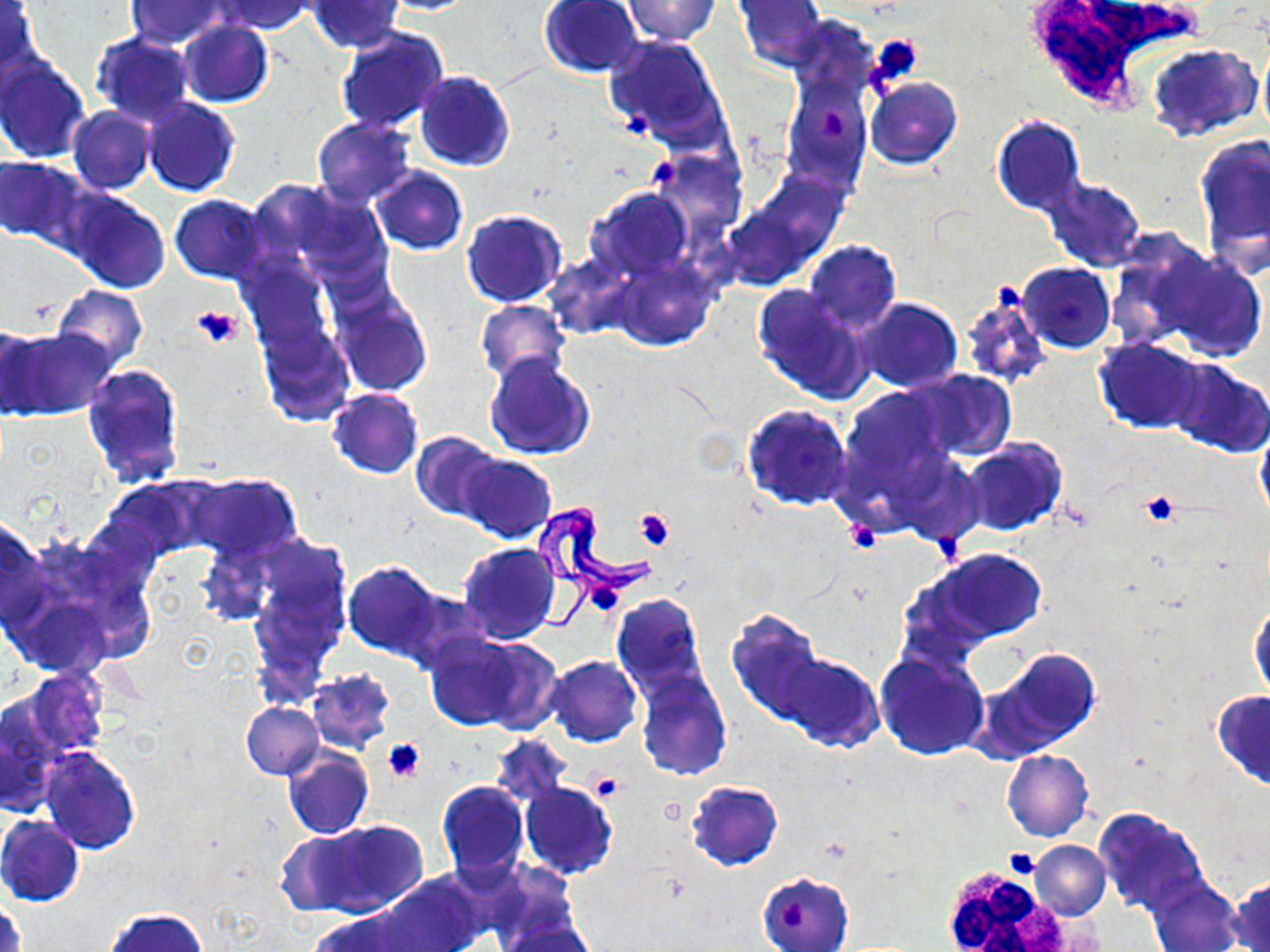

Summary:
  - Coordinate format: approximate bounding boxes as (x1,y1)-(x2,y2) corner pairs in pixels
  - Platelet locations: (866,34)-(921,91), (623,107)-(654,136), (824,109)-(845,138), (648,158)-(680,186), (994,282)-(1023,311), (192,304)-(245,349), (1139,490)-(1183,528), (635,508)-(676,549), (844,520)-(882,554), (933,532)-(965,559), (589,580)-(621,612), (383,739)-(425,782), (588,772)-(625,803), (656,799)-(686,826), (1003,847)-(1042,881), (780,897)-(812,931)
  - Uninfected red blood cell locations: (214,0)-(316,35), (376,0)-(481,15), (622,0)-(718,44), (732,0)-(828,72), (125,1)-(230,47), (307,1)-(405,53), (538,1)-(645,79), (1,2)-(42,79), (179,21)-(273,108), (335,27)-(450,135), (89,33)-(196,125), (604,34)-(726,149), (1257,36)-(1270,144), (1146,43)-(1261,144), (0,55)-(90,163), (784,59)-(871,194), (415,70)-(515,171), (865,78)-(963,170), (144,97)-(241,198), (66,107)-(155,194), (991,114)-(1086,216), (312,115)-(416,205), (1195,136)-(1269,268), (654,151)-(742,232), (0,156)-(83,246), (371,167)-(468,255), (1041,176)-(1146,271), (275,181)-(395,285), (586,185)-(695,283), (61,187)-(171,293), (170,195)-(267,284), (462,209)-(568,308), (1104,235)-(1223,349), (803,240)-(901,334), (1154,250)-(1267,361), (544,254)-(636,340), (241,255)-(336,357), (612,261)-(714,351), (1016,263)-(1117,354), (52,285)-(148,371), (752,285)-(873,404), (332,289)-(434,396), (959,290)-(1050,389), (857,299)-(962,391), (474,300)-(570,385), (258,322)-(354,427), (0,323)-(43,420), (5,328)-(118,419), (1094,337)-(1208,434), (483,352)-(596,460), (1166,359)-(1270,458), (83,363)-(187,489), (906,370)-(1016,462), (832,388)-(958,519), (328,389)-(423,479), (740,403)-(854,512), (1253,416)-(1270,528), (411,432)-(505,521), (961,438)-(1067,537), (458,453)-(556,543), (189,473)-(301,562), (103,476)-(211,561), (0,515)-(47,630), (459,542)-(559,644), (927,548)-(1047,644), (246,549)-(350,698), (342,560)-(444,660), (611,593)-(708,696), (1248,598)-(1269,701), (727,610)-(827,727), (434,633)-(562,734), (875,648)-(988,760), (979,648)-(1101,756), (775,653)-(882,751), (543,655)-(643,746), (20,668)-(109,758), (306,669)-(395,753), (635,671)-(731,781), (1212,690)-(1270,789), (242,703)-(323,779), (488,734)-(572,810), (38,747)-(141,854), (283,749)-(374,839), (1002,750)-(1093,841), (436,780)-(530,882), (519,781)-(618,879), (686,781)-(784,871), (1092,808)-(1209,916), (0,816)-(84,907), (301,819)-(427,918), (273,829)-(371,912), (1029,840)-(1110,920), (376,873)-(486,952), (757,873)-(853,952), (1146,874)-(1243,951), (1229,878)-(1270,951), (1,896)-(24,952), (107,908)-(207,952), (305,909)-(424,952), (496,912)-(597,952)
  - White blood cell locations: (1019,2)-(1202,118), (515,492)-(665,632), (941,868)-(1072,949)
  - Slide-level diagnosis: Trypanosoma brucei
  - Magnification: 1000x
  - Modality: light microscopy
  - Preparation: thin blood film
  - Field of view: one of a larger specimen
  - Image size: 1270×952 pixels
  - Stain: May-Grünwald-Giemsa